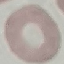
malaria_status: uninfected
image_type: automatically extracted cell patch, resized to 64 × 64 pixels
stain: Giemsa
preparation: thin blood smear
capture: smartphone camera at the microscope eyepiece